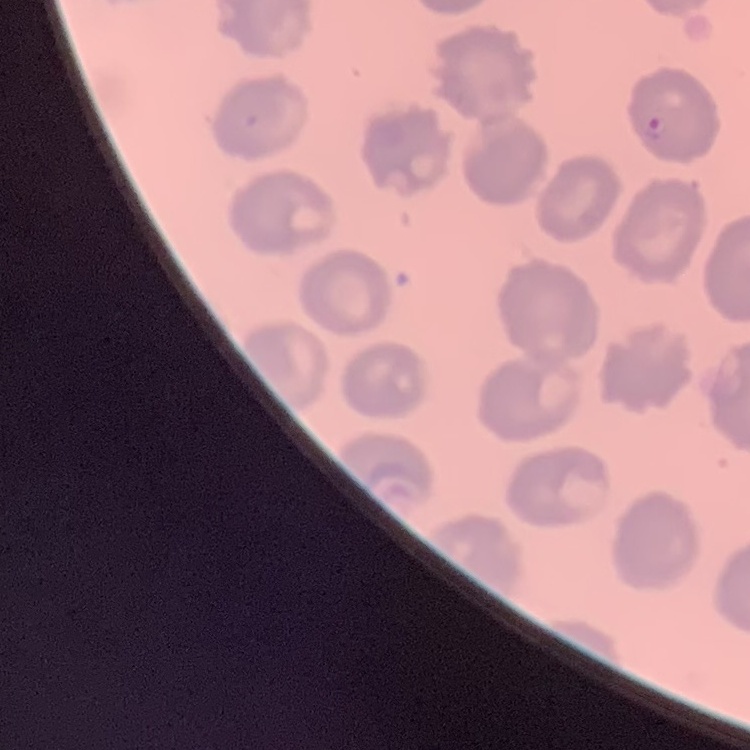
erythrocyte_morphology: no rouleaux formation
stain: Field's or Giemsa
image_type: square crop of a larger photomicrograph
preparation: thin blood film